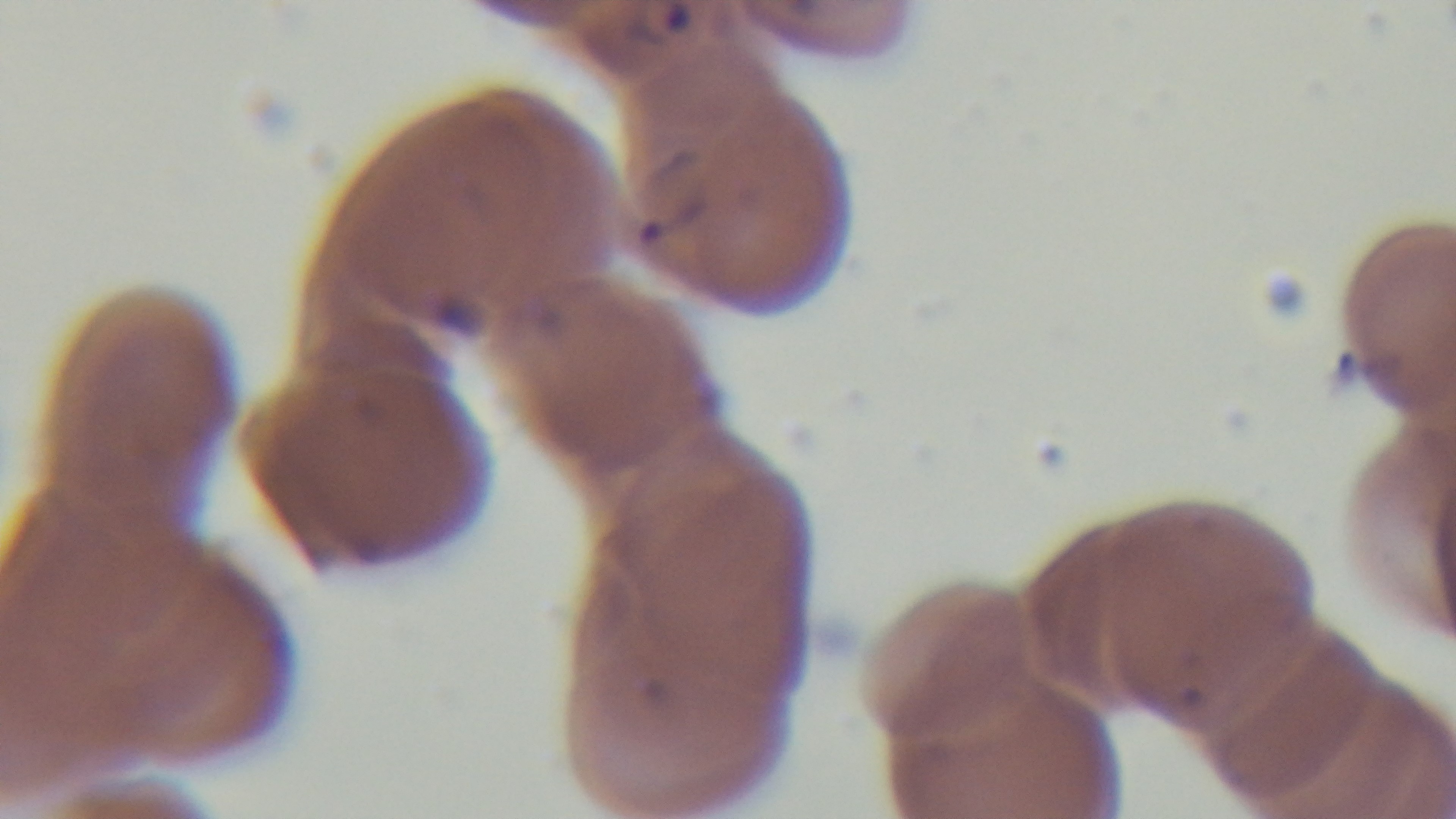
preparation = thin blood film
objective = 100x oil immersion
field of view = single
modality = light microscopy
malaria status = positive
stain = Giemsa
capture = mounted 4K digital camera